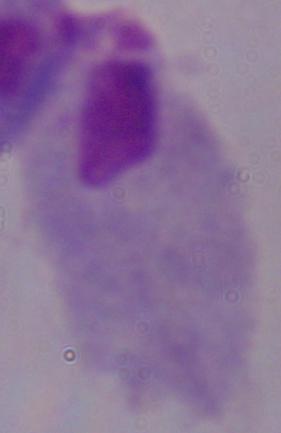
Summary:
  - Magnification: 1000x
  - Modality: micrograph
  - Identification: trichomonad